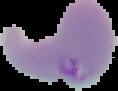

{
  "malaria_status": "parasitized",
  "image_type": "cell region segmented out of the field of view; surrounding area masked to black",
  "preparation": "thin blood smear",
  "image_size": "118×91 pixels"
}